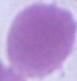

Summary:
  - Identification: erythrocyte
  - Modality: photomicrograph
  - Magnification: 1000x